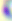
Summary:
  - Modality: micrograph
  - Identification: Toxoplasma gondii
  - Magnification: 400x